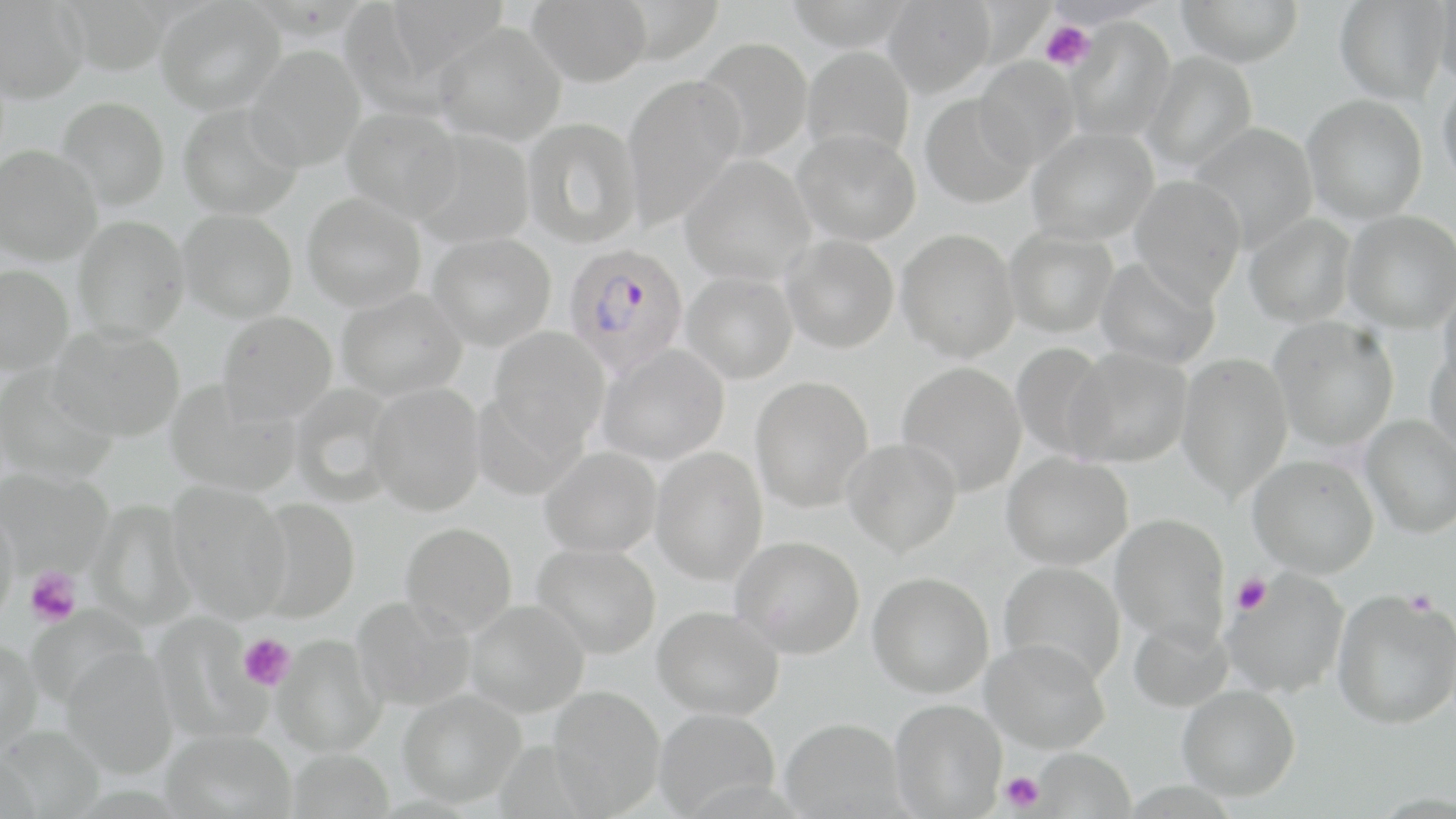

Summary:
  - Coordinate format: approximate bounding boxes as (x1,y1)-(x2,y2) corner pairs in pixels
  - Plasmodium falciparum-infected red blood cell locations: (564,243)-(689,375)
  - Platelet locations: (1040,21)-(1094,71), (25,568)-(81,626), (1232,573)-(1271,614), (1405,590)-(1439,616), (238,634)-(295,692), (1000,770)-(1044,813)
  - Uninfected red blood cell locations: (154,0)-(284,115), (527,0)-(652,87), (884,0)-(995,97), (1043,0)-(1164,28), (1177,0)-(1304,66), (1335,0)-(1449,104), (1435,0)-(1456,86), (0,1)-(88,103), (382,1)-(510,81), (1065,18)-(1175,142), (433,22)-(567,145), (694,37)-(813,163), (245,44)-(366,172), (801,45)-(915,163), (1141,52)-(1258,172), (974,56)-(1080,169), (1437,72)-(1456,191), (622,73)-(745,229), (920,94)-(1036,209), (1302,94)-(1427,224), (57,97)-(170,210), (178,102)-(304,220), (341,106)-(463,222), (523,117)-(643,247), (1186,123)-(1319,251), (1027,127)-(1158,245), (412,130)-(536,248), (793,130)-(921,245), (0,145)-(103,264), (680,154)-(816,286), (1129,175)-(1247,302), (302,191)-(427,312), (178,209)-(297,322), (1343,210)-(1456,333), (1244,213)-(1357,329), (73,216)-(190,341), (1004,227)-(1119,338), (897,228)-(1020,361), (428,233)-(556,351), (781,235)-(899,353), (1095,256)-(1220,370), (0,263)-(74,375), (681,271)-(798,383), (1438,282)-(1456,388), (335,288)-(468,401), (217,310)-(337,423), (1270,316)-(1399,451), (48,324)-(185,442), (489,326)-(611,449), (1010,341)-(1116,462), (1426,342)-(1456,457), (597,344)-(729,465), (1064,346)-(1193,467), (1176,352)-(1293,499), (896,361)-(1027,497), (0,366)-(119,484), (750,375)-(874,512), (164,380)-(301,497), (366,383)-(486,515), (290,384)-(401,506), (471,390)-(585,501), (1361,415)-(1456,538), (842,437)-(962,556), (540,446)-(662,557), (651,446)-(767,585), (1002,451)-(1132,569), (1247,453)-(1379,577), (0,468)-(114,578), (167,481)-(292,622), (250,498)-(361,623), (86,499)-(199,631), (0,503)-(19,628), (1110,513)-(1230,644), (400,521)-(518,636), (731,535)-(865,657), (532,542)-(661,659), (999,561)-(1126,684), (1222,569)-(1349,698), (868,571)-(995,698), (1332,589)-(1456,729), (352,596)-(476,711), (465,600)-(590,717), (25,605)-(147,710), (653,605)-(785,719), (150,612)-(266,744), (1127,616)-(1233,713), (272,634)-(387,757), (0,638)-(44,757), (981,638)-(1111,753), (60,647)-(179,779), (1176,684)-(1301,801), (548,685)-(666,816), (398,689)-(525,807), (890,698)-(1007,818), (654,708)-(780,816), (780,717)-(906,818), (0,724)-(106,817), (162,728)-(297,818), (287,747)-(394,819), (1031,748)-(1135,819)
  - Slide-level diagnosis: Plasmodium falciparum
  - Stain: May-Grünwald-Giemsa
  - Magnification: 1000x
  - Preparation: thin blood film
  - Field of view: one of a larger specimen
  - Image size: 1456×819 pixels
  - Modality: optical microscopy